Identify the preparation type.
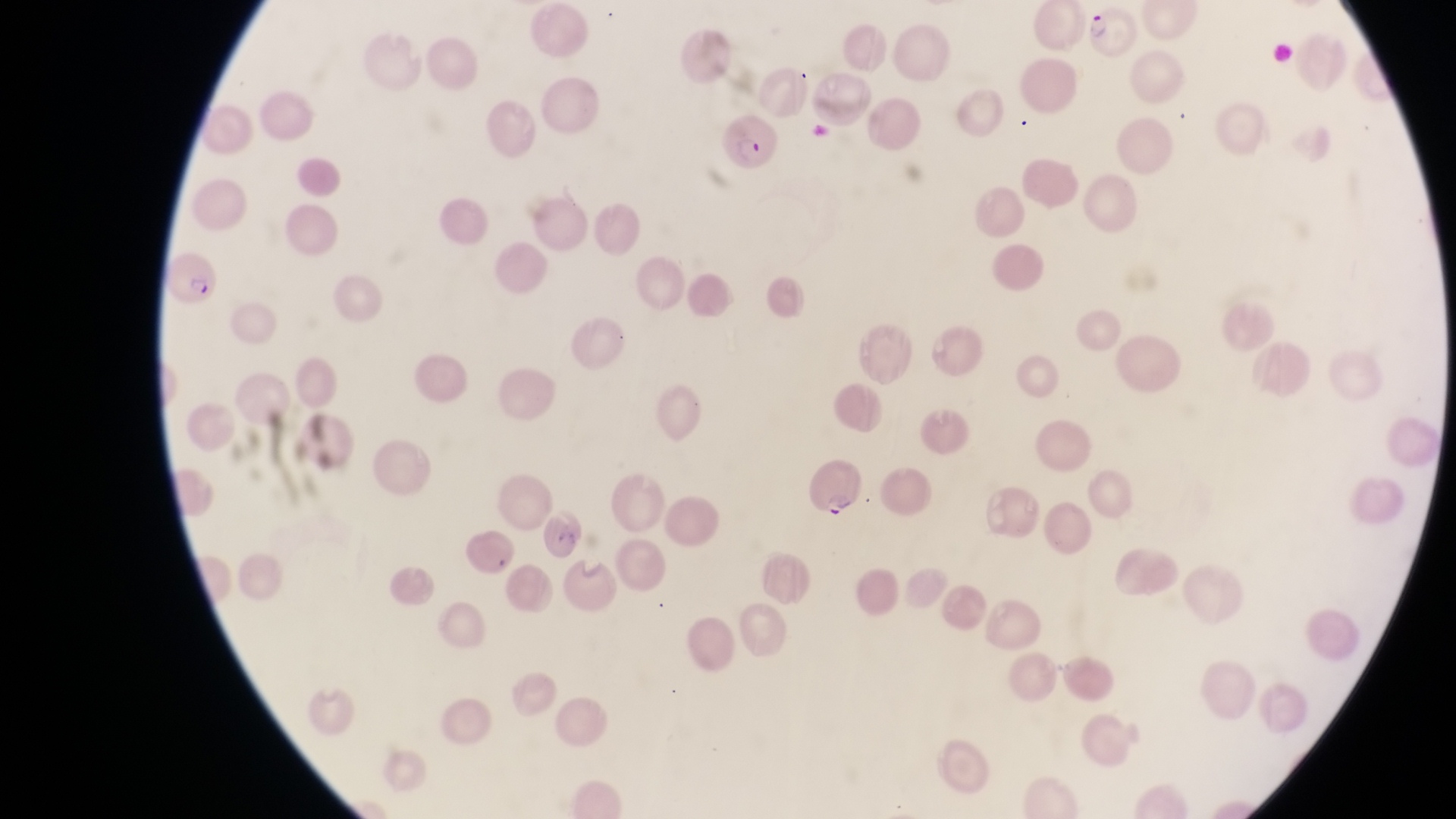

Thin blood smear.

Approximate bounding boxes as [left, top, right, bottom] in pixels. Parasitised red blood cell locations: [1086, 6, 1141, 61], [716, 112, 777, 181], [165, 248, 224, 311], [806, 457, 864, 523]. One field of view. Photographed through the eyepiece of an Olympus CX-23 microscope with a smartphone camera. Magnification of 1000x. Image is 1456×819 pixels. Collected in Uganda.